State which cell type is depicted.
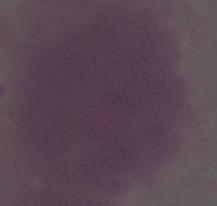

This is an erythrocyte.

Summary:
  - Modality: photomicrograph
  - Magnification: 1000x